Comment on the morphology of the red blood cells.
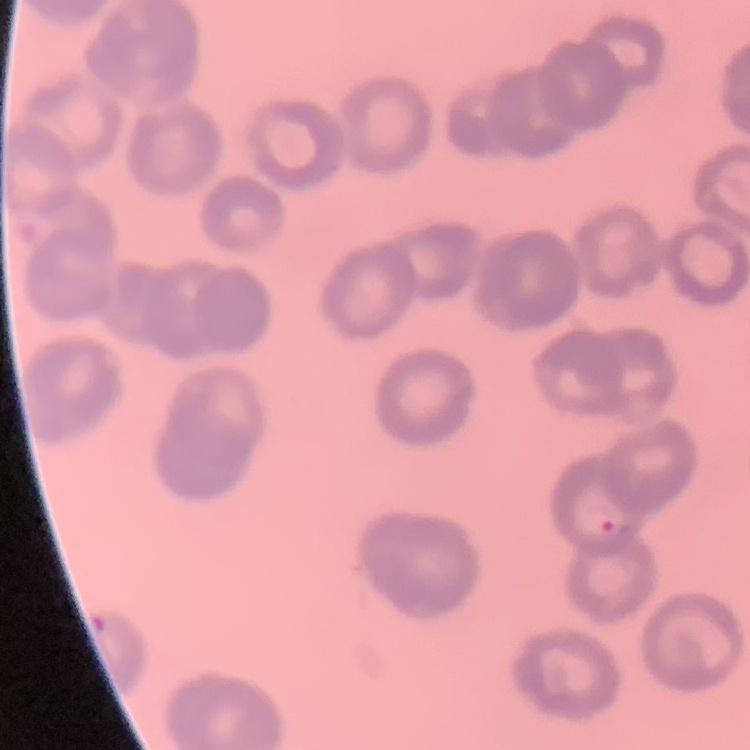
Rouleaux formation.

preparation = thin blood film
image type = one tile cut from a larger photomicrograph
stain = Field's or Giemsa